State which parasite is depicted.
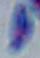

Toxoplasma gondii.

1000x magnification. Micrograph.